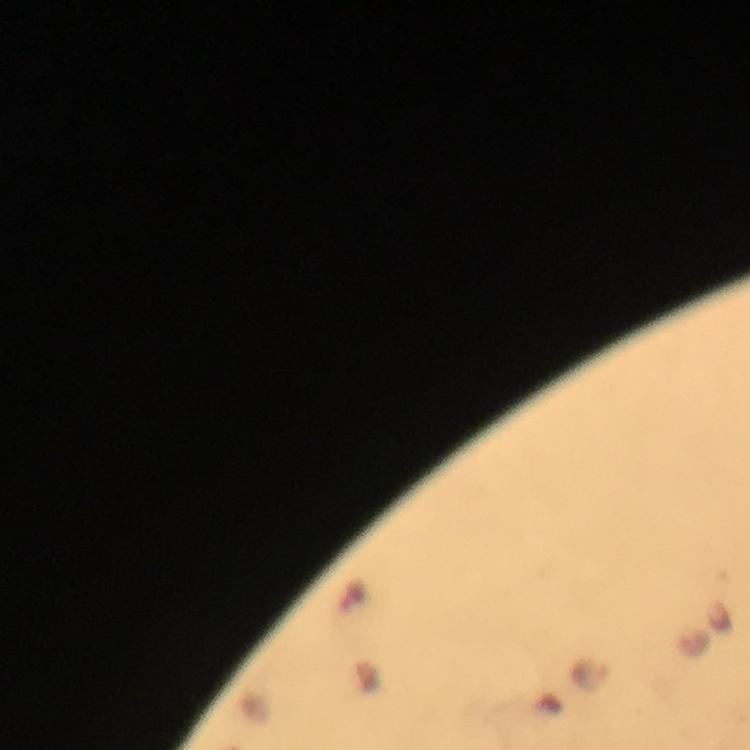

Approximate object centers, in pixels from the top-left corner.
Summary:
  - Malaria parasite locations: (x=589, y=677)
  - Capture: smartphone photograph through a microscope
  - Magnification: 100x
  - Context: from a malaria diagnostic workup
  - Cropped from: a single field of view
  - Preparation: thick blood smear
  - Immersion oil: used
  - Image size: 750×750 pixels
  - Stain: Giemsa